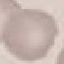
Summary:
  - Result: no malaria parasites seen
  - Stain: Giemsa
  - Preparation: thin smear
  - Capture: smartphone through the microscope eyepiece
  - Image type: cell patch, automatically extracted from a larger field of view and resized to 64 × 64 pixels